State the preparation type.
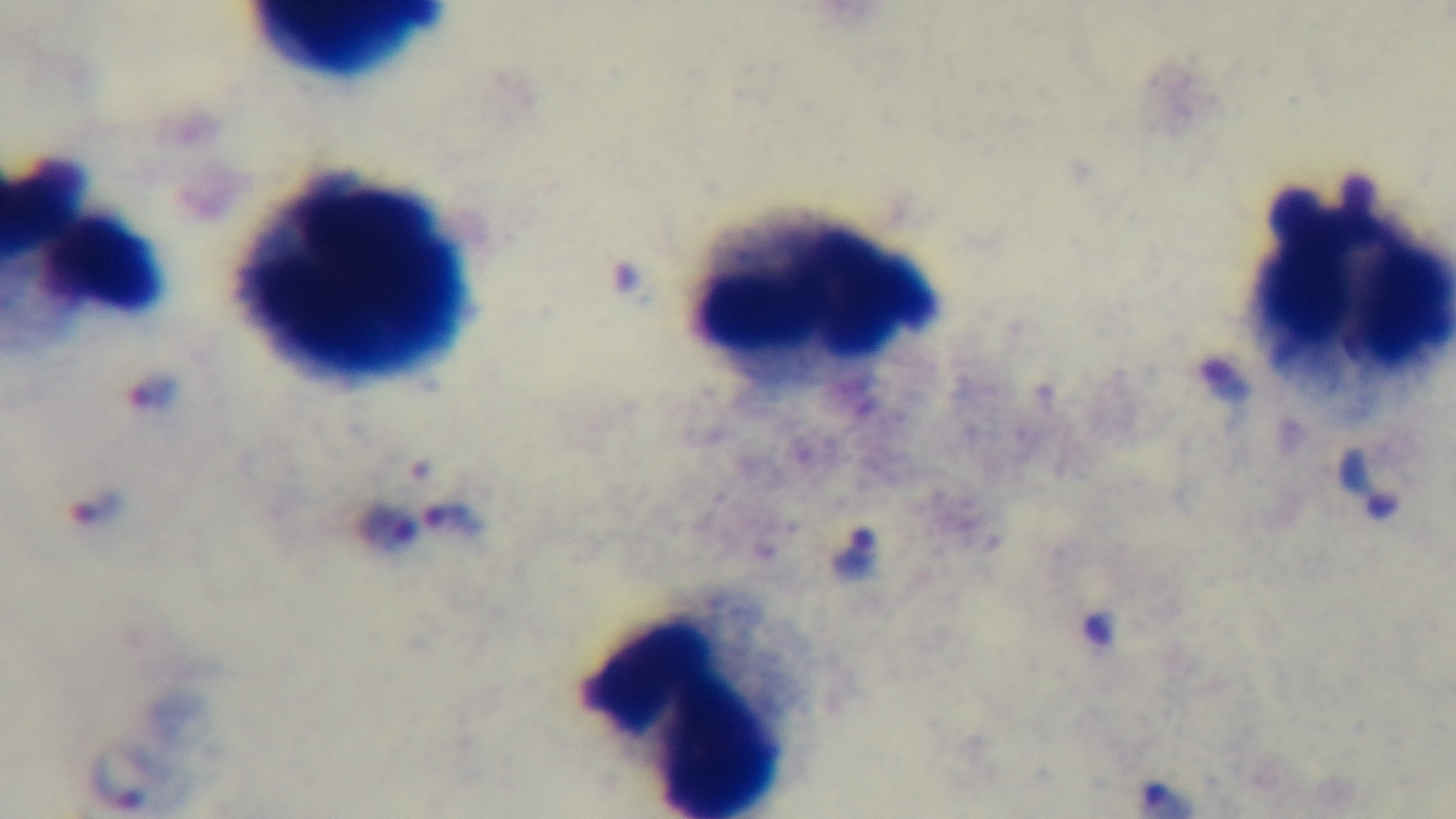

It is a thick blood film.

Summary:
  - Field of view: one from the slide
  - Objective: 100x oil immersion
  - Capture: mounted 4K digital camera
  - Malaria status: infected
  - Modality: light microscopy
  - Stain: Giemsa